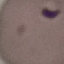 Malaria status: uninfected. Giemsa-stained preparation. Automatically extracted cell patch, resized to 64 × 64 pixels. Thin blood smear. Acquired by smartphone through the microscope eyepiece.